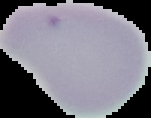

Image is 151×118 pixels. Result: no Plasmodium parasites detected. From a thin blood film. Segmented cell region on a black background.